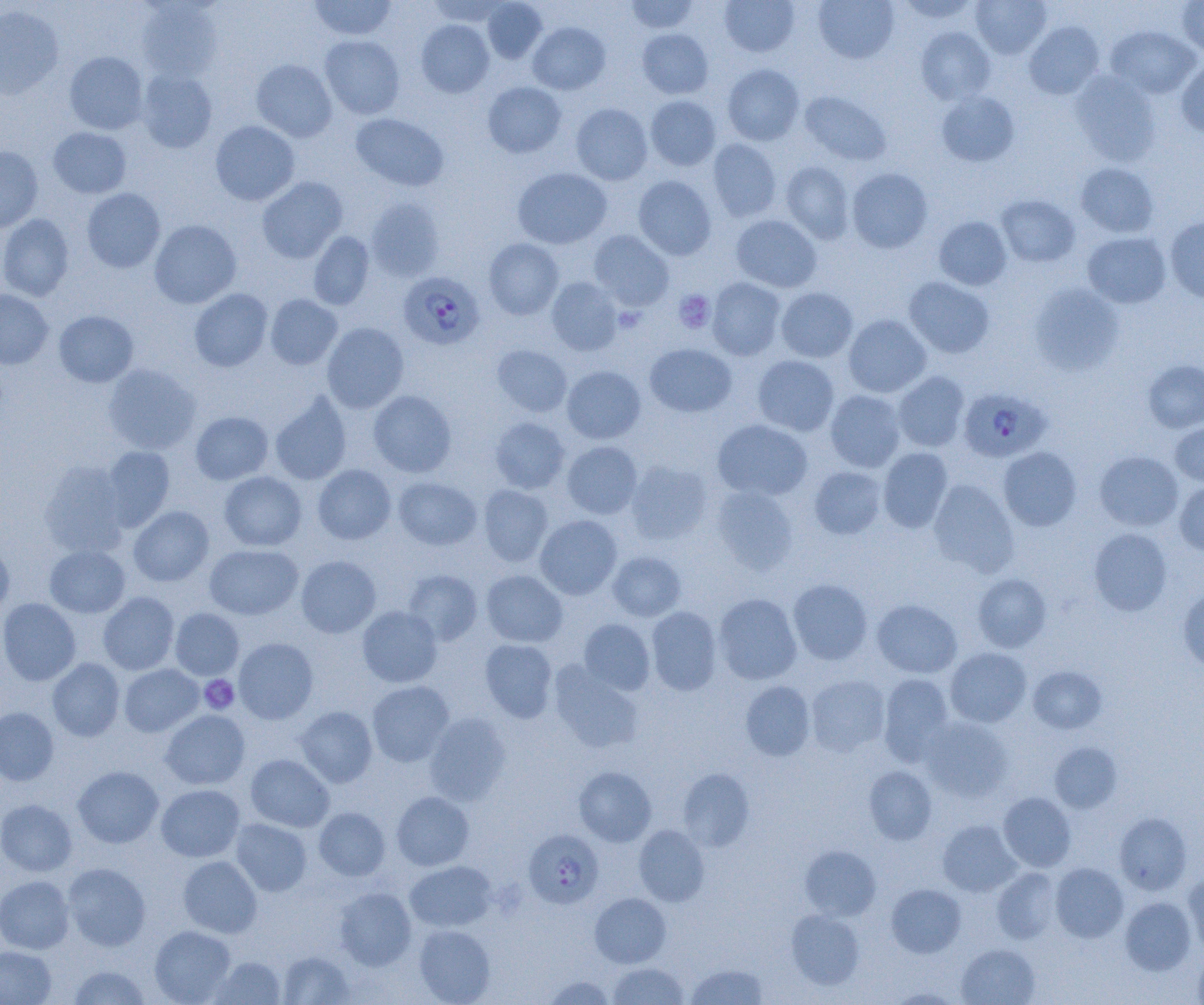

slide_level_diagnosis: Plasmodium falciparum
uninfected_red_blood_cell_locations: 'approximate bounding boxes as named x1/y1/x2/y2 corners in pixels: (x1=309, y1=0, x2=397, y2=41), (x1=426, y1=0, x2=510, y2=26), (x1=482, y1=0, x2=547, y2=63), (x1=624, y1=0, x2=700, y2=33), (x1=719, y1=0, x2=799, y2=57), (x1=813, y1=0, x2=899, y2=64), (x1=895, y1=0, x2=981, y2=24), (x1=970, y1=0, x2=1052, y2=59), (x1=1177, y1=1, x2=1204, y2=57), (x1=136, y1=2, x2=223, y2=82), (x1=0, y1=6, x2=64, y2=100), (x1=416, y1=20, x2=495, y2=97), (x1=1024, y1=21, x2=1104, y2=99), (x1=528, y1=22, x2=610, y2=94), (x1=1105, y1=25, x2=1201, y2=99), (x1=915, y1=27, x2=996, y2=105), (x1=637, y1=28, x2=713, y2=99), (x1=320, y1=35, x2=405, y2=120), (x1=64, y1=51, x2=148, y2=134), (x1=251, y1=59, x2=336, y2=142), (x1=1176, y1=59, x2=1204, y2=137), (x1=722, y1=64, x2=805, y2=145), (x1=136, y1=68, x2=217, y2=153), (x1=1070, y1=71, x2=1161, y2=166), (x1=483, y1=81, x2=566, y2=158), (x1=799, y1=91, x2=892, y2=166), (x1=936, y1=91, x2=1020, y2=167), (x1=645, y1=95, x2=721, y2=171), (x1=570, y1=103, x2=653, y2=185), (x1=351, y1=113, x2=449, y2=191), (x1=210, y1=120, x2=300, y2=206), (x1=48, y1=127, x2=131, y2=198), (x1=708, y1=138, x2=782, y2=222), (x1=0, y1=146, x2=43, y2=232), (x1=780, y1=160, x2=855, y2=243), (x1=1075, y1=163, x2=1159, y2=238), (x1=512, y1=167, x2=612, y2=249), (x1=846, y1=167, x2=933, y2=253), (x1=633, y1=175, x2=716, y2=260), (x1=257, y1=176, x2=348, y2=263), (x1=82, y1=188, x2=165, y2=273), (x1=996, y1=194, x2=1080, y2=267), (x1=365, y1=198, x2=445, y2=281), (x1=0, y1=214, x2=73, y2=301), (x1=731, y1=214, x2=822, y2=292), (x1=934, y1=216, x2=1012, y2=290), (x1=1165, y1=216, x2=1204, y2=303), (x1=149, y1=219, x2=241, y2=308), (x1=589, y1=230, x2=674, y2=311), (x1=308, y1=231, x2=374, y2=310), (x1=1082, y1=232, x2=1171, y2=308), (x1=484, y1=238, x2=563, y2=320), (x1=904, y1=276, x2=995, y2=358), (x1=546, y1=277, x2=623, y2=356), (x1=707, y1=278, x2=787, y2=361), (x1=1029, y1=284, x2=1125, y2=375), (x1=776, y1=287, x2=858, y2=362), (x1=189, y1=288, x2=273, y2=371), (x1=0, y1=289, x2=53, y2=369), (x1=265, y1=294, x2=342, y2=369), (x1=54, y1=310, x2=139, y2=387), (x1=843, y1=314, x2=931, y2=397), (x1=322, y1=322, x2=409, y2=413), (x1=645, y1=343, x2=736, y2=417), (x1=492, y1=344, x2=572, y2=417), (x1=752, y1=355, x2=839, y2=436), (x1=1142, y1=360, x2=1204, y2=432), (x1=102, y1=363, x2=200, y2=454), (x1=562, y1=365, x2=646, y2=444), (x1=892, y1=371, x2=969, y2=452), (x1=368, y1=390, x2=456, y2=477), (x1=825, y1=390, x2=907, y2=472), (x1=270, y1=391, x2=352, y2=484), (x1=190, y1=411, x2=273, y2=484), (x1=490, y1=417, x2=570, y2=493), (x1=712, y1=419, x2=813, y2=501), (x1=1169, y1=423, x2=1204, y2=486), (x1=562, y1=441, x2=642, y2=519), (x1=101, y1=446, x2=175, y2=530), (x1=878, y1=447, x2=953, y2=533), (x1=998, y1=447, x2=1082, y2=530), (x1=1094, y1=450, x2=1183, y2=531), (x1=625, y1=460, x2=713, y2=544), (x1=39, y1=461, x2=129, y2=557), (x1=312, y1=464, x2=396, y2=544), (x1=808, y1=466, x2=888, y2=539), (x1=218, y1=471, x2=307, y2=551), (x1=393, y1=476, x2=482, y2=550), (x1=928, y1=479, x2=1019, y2=576), (x1=1175, y1=481, x2=1204, y2=556), (x1=479, y1=484, x2=553, y2=567), (x1=710, y1=484, x2=799, y2=574), (x1=128, y1=505, x2=214, y2=586), (x1=535, y1=515, x2=622, y2=599), (x1=1088, y1=527, x2=1173, y2=616), (x1=0, y1=543, x2=14, y2=615), (x1=204, y1=544, x2=303, y2=620), (x1=45, y1=545, x2=130, y2=618), (x1=607, y1=550, x2=686, y2=621), (x1=296, y1=555, x2=381, y2=638), (x1=403, y1=569, x2=483, y2=645), (x1=481, y1=570, x2=567, y2=647), (x1=972, y1=573, x2=1052, y2=652), (x1=787, y1=578, x2=873, y2=665), (x1=1177, y1=586, x2=1204, y2=672), (x1=98, y1=592, x2=179, y2=675), (x1=714, y1=593, x2=802, y2=684), (x1=0, y1=597, x2=81, y2=685), (x1=871, y1=599, x2=962, y2=678), (x1=357, y1=605, x2=443, y2=687), (x1=646, y1=606, x2=722, y2=695), (x1=170, y1=607, x2=244, y2=679), (x1=578, y1=619, x2=655, y2=696), (x1=234, y1=637, x2=318, y2=723), (x1=480, y1=639, x2=557, y2=722), (x1=945, y1=647, x2=1031, y2=727), (x1=47, y1=657, x2=125, y2=741), (x1=549, y1=660, x2=645, y2=753), (x1=119, y1=664, x2=203, y2=736), (x1=1028, y1=665, x2=1107, y2=734), (x1=806, y1=674, x2=891, y2=757), (x1=878, y1=674, x2=954, y2=764), (x1=366, y1=680, x2=455, y2=766), (x1=740, y1=680, x2=815, y2=761), (x1=295, y1=705, x2=377, y2=787), (x1=0, y1=707, x2=59, y2=785), (x1=160, y1=709, x2=250, y2=789), (x1=424, y1=712, x2=511, y2=805), (x1=920, y1=717, x2=1013, y2=801), (x1=1049, y1=742, x2=1121, y2=813), (x1=245, y1=754, x2=334, y2=832), (x1=864, y1=765, x2=937, y2=844), (x1=72, y1=766, x2=163, y2=848), (x1=574, y1=766, x2=656, y2=846), (x1=677, y1=768, x2=754, y2=851), (x1=155, y1=784, x2=245, y2=861), (x1=391, y1=791, x2=474, y2=870), (x1=998, y1=792, x2=1076, y2=872), (x1=0, y1=799, x2=77, y2=876), (x1=314, y1=807, x2=390, y2=880), (x1=1114, y1=812, x2=1192, y2=895), (x1=230, y1=819, x2=312, y2=896), (x1=937, y1=820, x2=1021, y2=896), (x1=633, y1=824, x2=710, y2=906), (x1=800, y1=845, x2=881, y2=920), (x1=178, y1=855, x2=263, y2=938), (x1=405, y1=860, x2=497, y2=931), (x1=62, y1=862, x2=151, y2=951), (x1=1050, y1=863, x2=1128, y2=942), (x1=992, y1=867, x2=1061, y2=944), (x1=1183, y1=871, x2=1204, y2=955), (x1=0, y1=875, x2=74, y2=954), (x1=886, y1=883, x2=966, y2=957), (x1=334, y1=887, x2=417, y2=970), (x1=590, y1=893, x2=671, y2=968), (x1=1120, y1=896, x2=1197, y2=975), (x1=786, y1=909, x2=865, y2=990), (x1=413, y1=924, x2=495, y2=1004), (x1=149, y1=925, x2=236, y2=1004), (x1=956, y1=943, x2=1040, y2=1005), (x1=0, y1=946, x2=56, y2=1005), (x1=1193, y1=949, x2=1204, y2=1005), (x1=277, y1=950, x2=355, y2=1004), (x1=209, y1=956, x2=286, y2=1004), (x1=607, y1=962, x2=689, y2=1005), (x1=686, y1=963, x2=768, y2=1004), (x1=68, y1=965, x2=151, y2=1004), (x1=541, y1=975, x2=616, y2=1004), (x1=888, y1=987, x2=964, y2=1004)'
platelet_locations: 'approximate bounding boxes as named x1/y1/x2/y2 corners in pixels: (x1=673, y1=290, x2=715, y2=333), (x1=612, y1=306, x2=646, y2=333), (x1=199, y1=675, x2=239, y2=714)'
image_size: 1204×1005 pixels
magnification: 1000x
field_of_view: one of a larger specimen
plasmodium_falciparum_infected_red_blood_cell_locations: 'approximate bounding boxes as named x1/y1/x2/y2 corners in pixels: (x1=398, y1=271, x2=484, y2=350), (x1=959, y1=387, x2=1050, y2=463), (x1=523, y1=829, x2=604, y2=908)'
modality: light microscopy
preparation: thin blood film